Comment on the morphology of the erythrocytes.
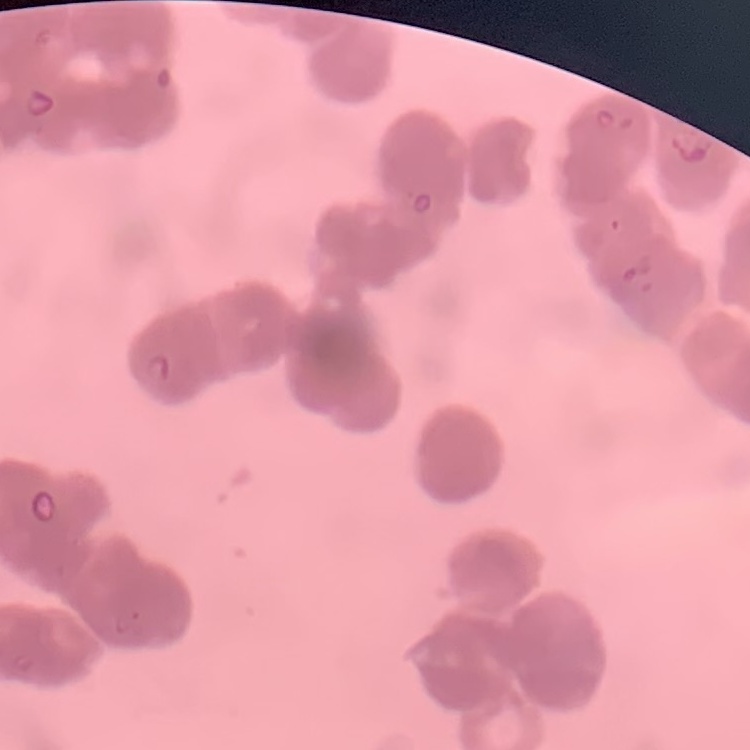
Rouleaux formation.

Summary:
  - Stain: Field's or Giemsa
  - Preparation: thin blood film
  - Image type: one tile cut from a larger photomicrograph